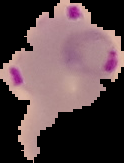
Summary:
  - Preparation: thin blood film
  - Image size: 124×163 pixels
  - Malaria status: parasitized
  - Image type: cell region segmented out of the field of view; surrounding area masked to black